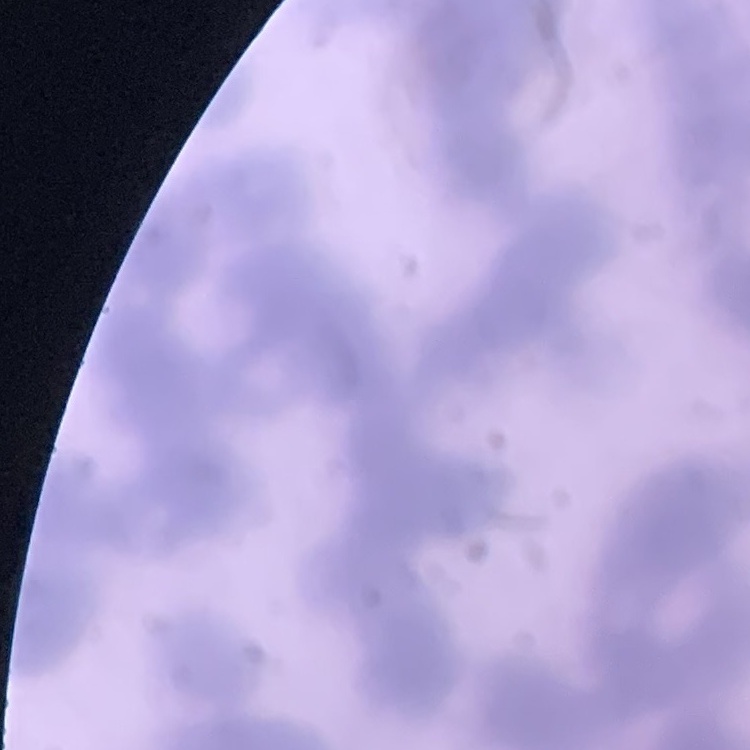

The erythrocytes exhibit rouleaux formation. One tile cut from a larger photomicrograph. Field's or Giemsa stain. Thin blood smear.